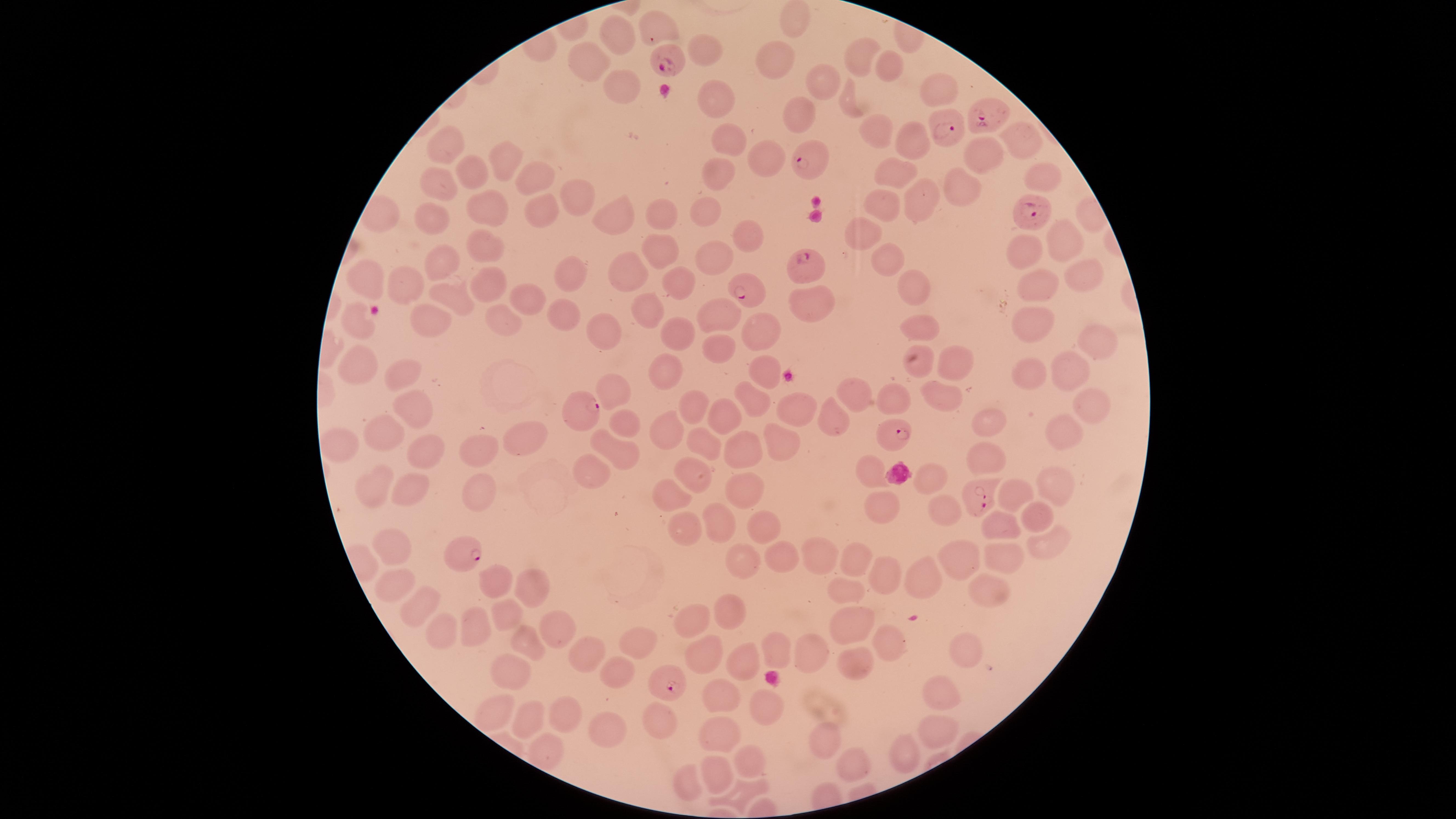

capture = smartphone photograph through the microscope eyepiece
stain = Giemsa
visible region = circular
field of view = single
species = Plasmodium falciparum
image size = 1456×819 pixels
presence = malaria parasites identified
preparation = thin smear of blood
uninfected red blood cells = approximate marker points as (x, y) in pixels: (796, 21), (655, 25), (613, 40), (706, 50), (856, 56), (588, 61), (778, 63), (886, 67), (821, 78), (618, 86), (942, 92), (719, 99), (848, 103), (799, 115), (729, 133), (1020, 135), (912, 142), (448, 150), (982, 155), (508, 156), (766, 162), (1151, 162), (480, 169), (898, 173), (1045, 174), (536, 175), (719, 175), (439, 179), (963, 185), (578, 193), (919, 199), (706, 204), (487, 206), (888, 207), (545, 211), (656, 213), (430, 216), (622, 219), (874, 231), (748, 237), (1063, 241), (658, 253), (718, 253), (1030, 253), (485, 254), (888, 256), (443, 261), (569, 272), (634, 272), (1084, 276), (909, 277), (370, 279), (488, 280), (404, 282), (684, 282), (1035, 286), (452, 293), (819, 299), (530, 303), (564, 309), (645, 310), (721, 313), (431, 317), (501, 319), (1035, 319), (359, 320), (760, 327), (925, 330), (685, 332), (602, 335), (1094, 339), (713, 345), (954, 361), (921, 362), (357, 365), (1067, 365), (764, 368), (665, 370), (1026, 371), (396, 373), (612, 385), (939, 387), (860, 390), (753, 396), (896, 398), (1085, 399), (419, 400), (694, 404), (804, 405), (722, 410), (832, 413), (624, 421), (991, 423), (1060, 426), (668, 430), (386, 432), (524, 438), (780, 441), (708, 445), (342, 446), (747, 446), (423, 452), (615, 453), (480, 455), (986, 458), (869, 469), (589, 470), (696, 475), (929, 475), (1050, 481), (372, 484), (747, 484), (409, 488), (481, 493), (667, 493), (1012, 493), (875, 504), (938, 510), (1030, 517), (716, 521), (1000, 525), (682, 526), (761, 526), (391, 544), (1045, 544), (815, 552), (741, 558), (777, 558), (856, 559), (958, 561), (994, 561), (884, 574), (929, 576), (497, 578), (390, 583), (525, 585), (847, 585), (988, 588), (425, 603), (729, 610), (505, 612), (848, 619), (690, 623), (470, 626), (441, 628), (555, 630), (884, 638), (636, 642), (531, 644), (582, 648), (776, 648), (812, 652), (966, 653), (700, 657), (738, 657), (856, 664), (618, 669), (513, 672), (940, 692), (716, 696), (494, 708), (758, 708), (562, 713), (657, 720), (528, 721), (602, 725), (939, 726), (720, 733), (822, 739), (541, 746), (906, 752), (751, 759), (852, 766), (714, 768), (684, 778), (742, 790)
parasitized red blood cells = approximate marker points as (x, y) in pixels: (664, 60), (985, 116), (949, 132), (805, 163), (1024, 209), (808, 264), (744, 289), (582, 412), (894, 433), (982, 496), (461, 556), (671, 684)